State the blood parasite species.
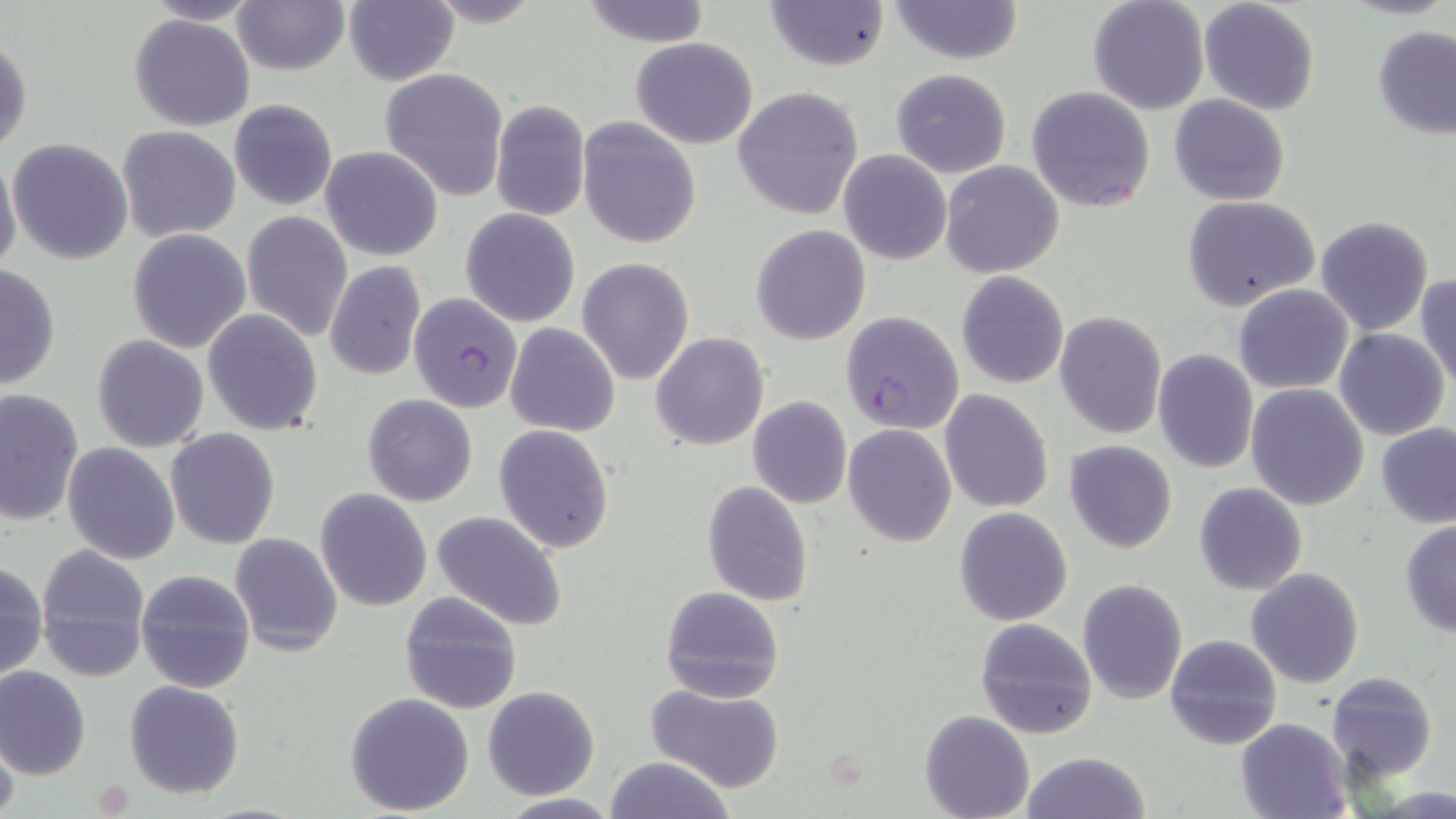

Plasmodium falciparum.

Summary:
  - Coordinate format: approximate bounding boxes as [x1, y1, x2, y2] in pixels
  - Plasmodium falciparum-infected red blood cell locations: [408, 291, 523, 414], [840, 312, 963, 433]
  - Uninfected red blood cell locations: [422, 0, 547, 29], [1087, 0, 1212, 115], [1198, 0, 1322, 116], [144, 1, 264, 25], [230, 1, 350, 74], [342, 1, 458, 86], [579, 1, 713, 47], [887, 1, 1023, 65], [766, 2, 888, 71], [129, 13, 254, 131], [1374, 28, 1456, 139], [1, 32, 32, 157], [630, 37, 759, 150], [595, 56, 733, 210], [380, 68, 508, 202], [890, 68, 1012, 178], [1026, 85, 1157, 213], [731, 86, 864, 220], [1170, 94, 1290, 206], [229, 99, 339, 210], [490, 101, 591, 221], [578, 117, 703, 249], [117, 125, 240, 242], [7, 137, 132, 265], [320, 145, 442, 261], [839, 150, 951, 265], [0, 151, 22, 280], [941, 160, 1065, 279], [1183, 197, 1321, 312], [461, 207, 580, 327], [241, 211, 353, 341], [1315, 215, 1434, 335], [750, 225, 871, 346], [126, 228, 251, 353], [577, 257, 695, 385], [323, 261, 427, 382], [0, 262, 61, 392], [1416, 271, 1456, 390], [955, 272, 1069, 389], [1233, 284, 1354, 393], [202, 310, 325, 436], [1054, 311, 1166, 438], [504, 323, 620, 438], [1333, 328, 1450, 441], [651, 332, 769, 451], [92, 335, 209, 453], [1152, 348, 1259, 474], [1245, 383, 1369, 511], [0, 388, 85, 527], [939, 390, 1053, 512], [362, 394, 477, 506], [748, 396, 852, 508], [1375, 422, 1456, 527], [493, 423, 615, 553], [844, 424, 957, 548], [165, 428, 280, 548], [1064, 440, 1178, 554], [62, 443, 180, 565], [702, 480, 814, 607], [1193, 482, 1308, 596], [316, 489, 433, 611], [954, 507, 1073, 625], [432, 510, 568, 631], [1399, 520, 1456, 637], [229, 533, 342, 657], [34, 544, 152, 680], [0, 558, 48, 683], [1246, 567, 1364, 688], [136, 568, 256, 691], [1078, 578, 1187, 704], [659, 586, 784, 703], [397, 590, 524, 715], [975, 618, 1098, 739], [1165, 634, 1283, 752], [1, 666, 91, 780], [1326, 672, 1437, 782], [124, 680, 244, 800], [643, 684, 788, 793], [482, 686, 600, 799], [344, 692, 475, 814], [920, 710, 1035, 819], [1236, 717, 1353, 818], [0, 730, 20, 819], [1019, 751, 1151, 819], [604, 756, 735, 819], [496, 793, 623, 818]
  - Modality: light microscopy
  - Stain: May-Grünwald-Giemsa
  - Image size: 1456×819 pixels
  - Magnification: 1000x
  - Field of view: single
  - Preparation: thin blood smear